Mark where platelets are.
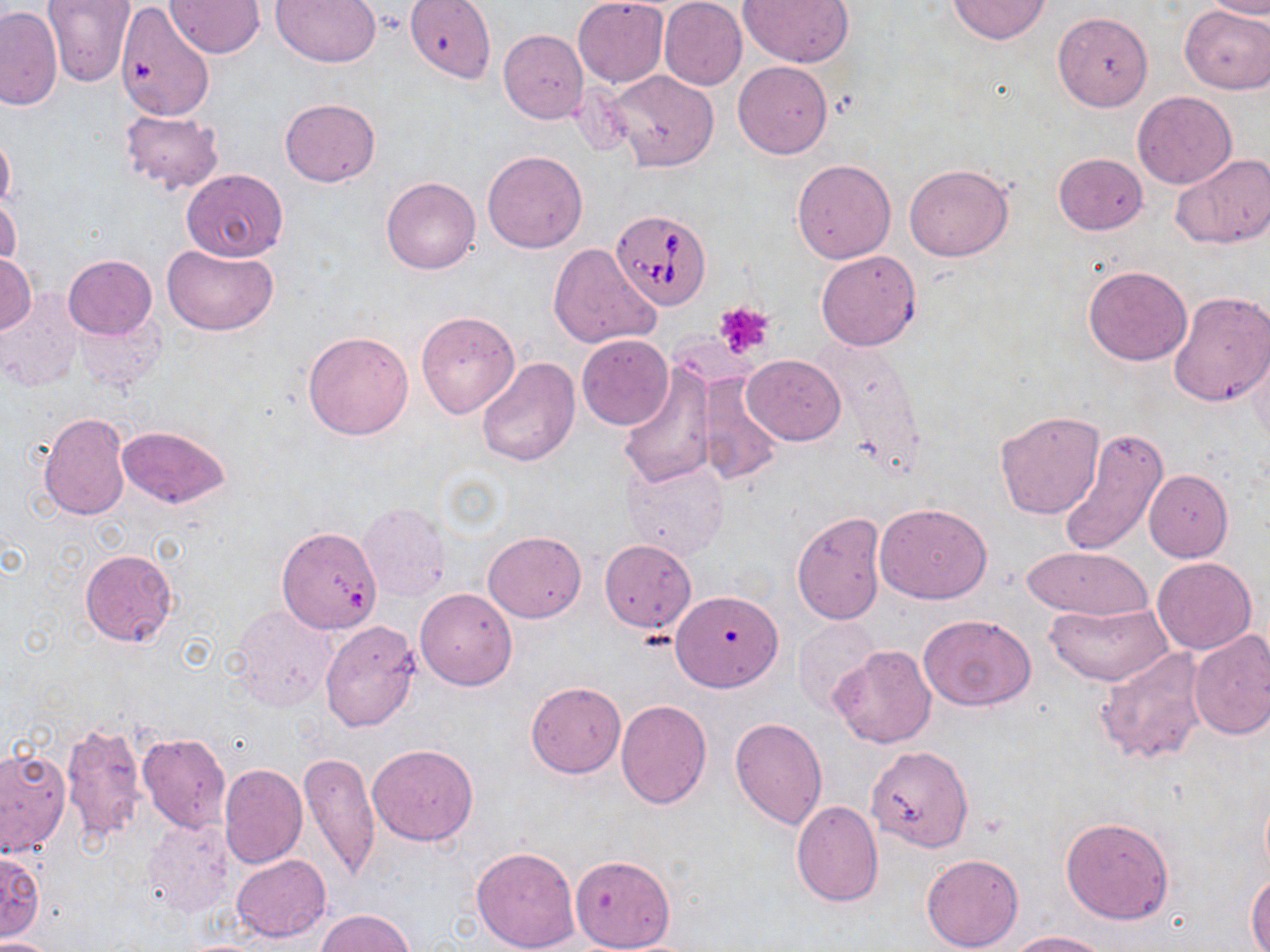
Approximate bounding boxes as named x1/y1/x2/y2 corners in pixels.
Platelets: (x1=716, y1=301, x2=774, y2=357).

slide-level diagnosis = Babesia divergens
uninfected red blood cell locations = approximate bounding boxes as named x1/y1/x2/y2 corners in pixels: (x1=42, y1=0, x2=137, y2=88), (x1=168, y1=0, x2=263, y2=56), (x1=271, y1=0, x2=382, y2=68), (x1=405, y1=0, x2=495, y2=80), (x1=573, y1=0, x2=668, y2=87), (x1=659, y1=0, x2=747, y2=90), (x1=739, y1=0, x2=854, y2=67), (x1=947, y1=0, x2=1054, y2=45), (x1=1203, y1=1, x2=1270, y2=20), (x1=1180, y1=5, x2=1269, y2=93), (x1=0, y1=6, x2=62, y2=110), (x1=118, y1=6, x2=214, y2=119), (x1=1052, y1=12, x2=1153, y2=111), (x1=498, y1=29, x2=589, y2=122), (x1=733, y1=61, x2=832, y2=159), (x1=604, y1=71, x2=719, y2=172), (x1=1132, y1=91, x2=1237, y2=188), (x1=280, y1=98, x2=380, y2=187), (x1=119, y1=108, x2=223, y2=195), (x1=0, y1=129, x2=15, y2=216), (x1=482, y1=151, x2=587, y2=253), (x1=1053, y1=152, x2=1147, y2=234), (x1=1170, y1=152, x2=1268, y2=249), (x1=792, y1=158, x2=897, y2=264), (x1=904, y1=163, x2=1013, y2=261), (x1=182, y1=168, x2=287, y2=261), (x1=381, y1=175, x2=480, y2=275), (x1=0, y1=195, x2=20, y2=275), (x1=163, y1=243, x2=278, y2=336), (x1=548, y1=243, x2=660, y2=351), (x1=1, y1=251, x2=36, y2=336), (x1=816, y1=251, x2=921, y2=351), (x1=63, y1=255, x2=156, y2=339), (x1=1083, y1=264, x2=1192, y2=365), (x1=0, y1=290, x2=83, y2=390), (x1=1169, y1=291, x2=1270, y2=407), (x1=72, y1=309, x2=166, y2=393), (x1=415, y1=311, x2=519, y2=418), (x1=303, y1=330, x2=414, y2=440), (x1=577, y1=334, x2=673, y2=430), (x1=1246, y1=339, x2=1269, y2=451), (x1=742, y1=355, x2=845, y2=445), (x1=477, y1=357, x2=580, y2=468), (x1=619, y1=365, x2=717, y2=488), (x1=695, y1=371, x2=784, y2=485), (x1=995, y1=410, x2=1105, y2=520), (x1=37, y1=412, x2=131, y2=521), (x1=117, y1=426, x2=230, y2=508), (x1=1057, y1=428, x2=1168, y2=557), (x1=622, y1=460, x2=730, y2=559), (x1=1144, y1=470, x2=1232, y2=561), (x1=358, y1=501, x2=451, y2=601), (x1=875, y1=502, x2=991, y2=603), (x1=792, y1=512, x2=886, y2=624), (x1=277, y1=526, x2=382, y2=634), (x1=483, y1=529, x2=586, y2=622), (x1=599, y1=540, x2=696, y2=632), (x1=1022, y1=545, x2=1156, y2=620), (x1=79, y1=548, x2=178, y2=648), (x1=1151, y1=556, x2=1257, y2=655), (x1=415, y1=588, x2=517, y2=690), (x1=671, y1=592, x2=781, y2=691), (x1=1045, y1=602, x2=1174, y2=686), (x1=230, y1=603, x2=337, y2=712), (x1=920, y1=615, x2=1035, y2=709), (x1=793, y1=618, x2=881, y2=715), (x1=320, y1=621, x2=420, y2=732), (x1=1187, y1=630, x2=1270, y2=740), (x1=829, y1=645, x2=937, y2=748), (x1=1095, y1=645, x2=1210, y2=766), (x1=526, y1=681, x2=626, y2=777), (x1=615, y1=699, x2=711, y2=809), (x1=730, y1=717, x2=829, y2=829), (x1=59, y1=722, x2=148, y2=847), (x1=137, y1=732, x2=231, y2=833), (x1=367, y1=744, x2=478, y2=847), (x1=866, y1=746, x2=973, y2=852), (x1=1, y1=748, x2=70, y2=855), (x1=296, y1=751, x2=381, y2=881), (x1=219, y1=763, x2=307, y2=868), (x1=790, y1=801, x2=883, y2=907), (x1=1060, y1=816, x2=1174, y2=923), (x1=141, y1=818, x2=237, y2=920), (x1=471, y1=846, x2=580, y2=952), (x1=1, y1=850, x2=45, y2=942), (x1=920, y1=852, x2=1024, y2=951), (x1=568, y1=853, x2=677, y2=951), (x1=231, y1=854, x2=331, y2=943), (x1=1247, y1=870, x2=1270, y2=952), (x1=315, y1=909, x2=417, y2=952), (x1=1004, y1=930, x2=1110, y2=951), (x1=0, y1=937, x2=55, y2=952)
Babesia divergens-infected red blood cell locations = approximate bounding boxes as named x1/y1/x2/y2 corners in pixels: (x1=612, y1=209, x2=713, y2=310)
modality = optical microscopy
preparation = thin blood film
stain = May-Grünwald-Giemsa
field of view = one of a larger specimen
image size = 1270×952 pixels
magnification = 1000x